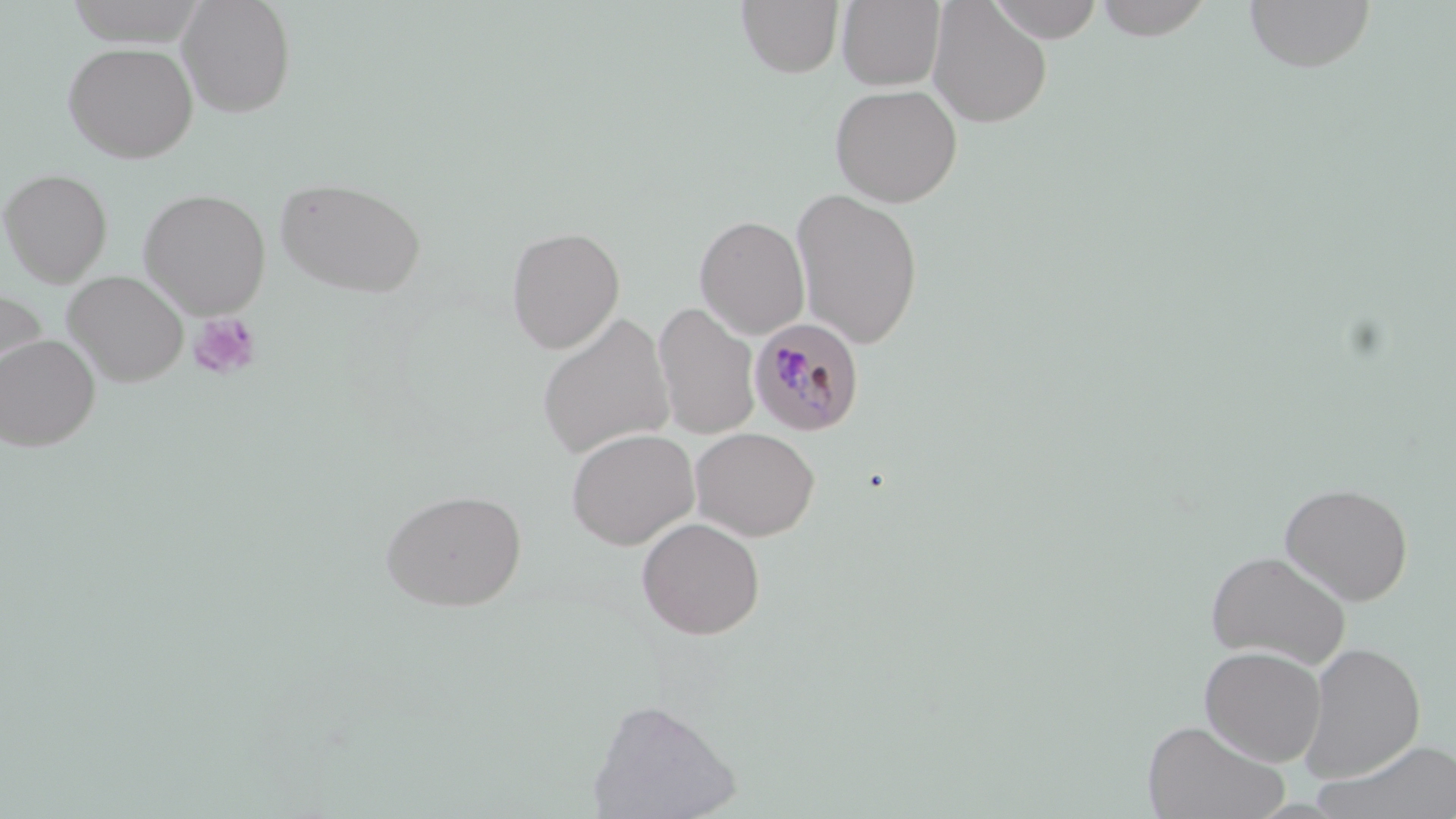

slide-level diagnosis = Plasmodium malariae
image size = 1456×819 pixels
stain = May-Grünwald-Giemsa
modality = light microscopy
uninfected red blood cell locations = approximate bounding boxes as (x1, y1, x2, y2) in pixels: (177, 0, 297, 118), (837, 0, 945, 91), (986, 0, 1105, 42), (1091, 0, 1216, 41), (1244, 0, 1376, 73), (736, 1, 843, 78), (928, 1, 1052, 127), (66, 2, 208, 46), (63, 41, 198, 163), (829, 83, 962, 207), (0, 168, 112, 285), (274, 176, 427, 297), (138, 188, 270, 317), (791, 188, 924, 349), (695, 215, 810, 339), (506, 226, 624, 353), (63, 271, 188, 387), (0, 286, 49, 386), (653, 302, 760, 439), (537, 313, 675, 460), (0, 334, 100, 451), (690, 427, 820, 540), (566, 428, 699, 549), (1278, 481, 1414, 605), (380, 489, 527, 611), (636, 517, 765, 639), (1204, 549, 1351, 669), (1299, 642, 1426, 782), (1199, 645, 1327, 766), (586, 698, 741, 818), (1142, 718, 1289, 819), (1308, 739, 1456, 819)
field of view = single
preparation = thin blood film
Plasmodium malariae-infected red blood cell locations = approximate bounding boxes as (x1, y1, x2, y2) in pixels: (749, 318, 865, 436)
magnification = 1000x
platelet locations = approximate bounding boxes as (x1, y1, x2, y2) in pixels: (187, 312, 262, 381)